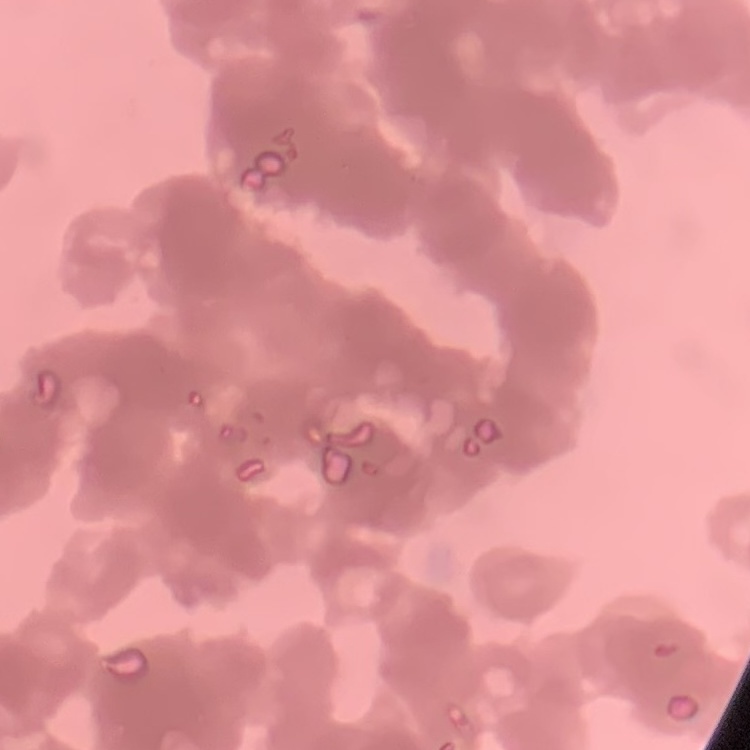

Summary:
  - Red blood cell morphology: rouleaux formation
  - Stain: Field's or Giemsa
  - Preparation: thin blood smear
  - Image type: one tile cut from a larger photomicrograph